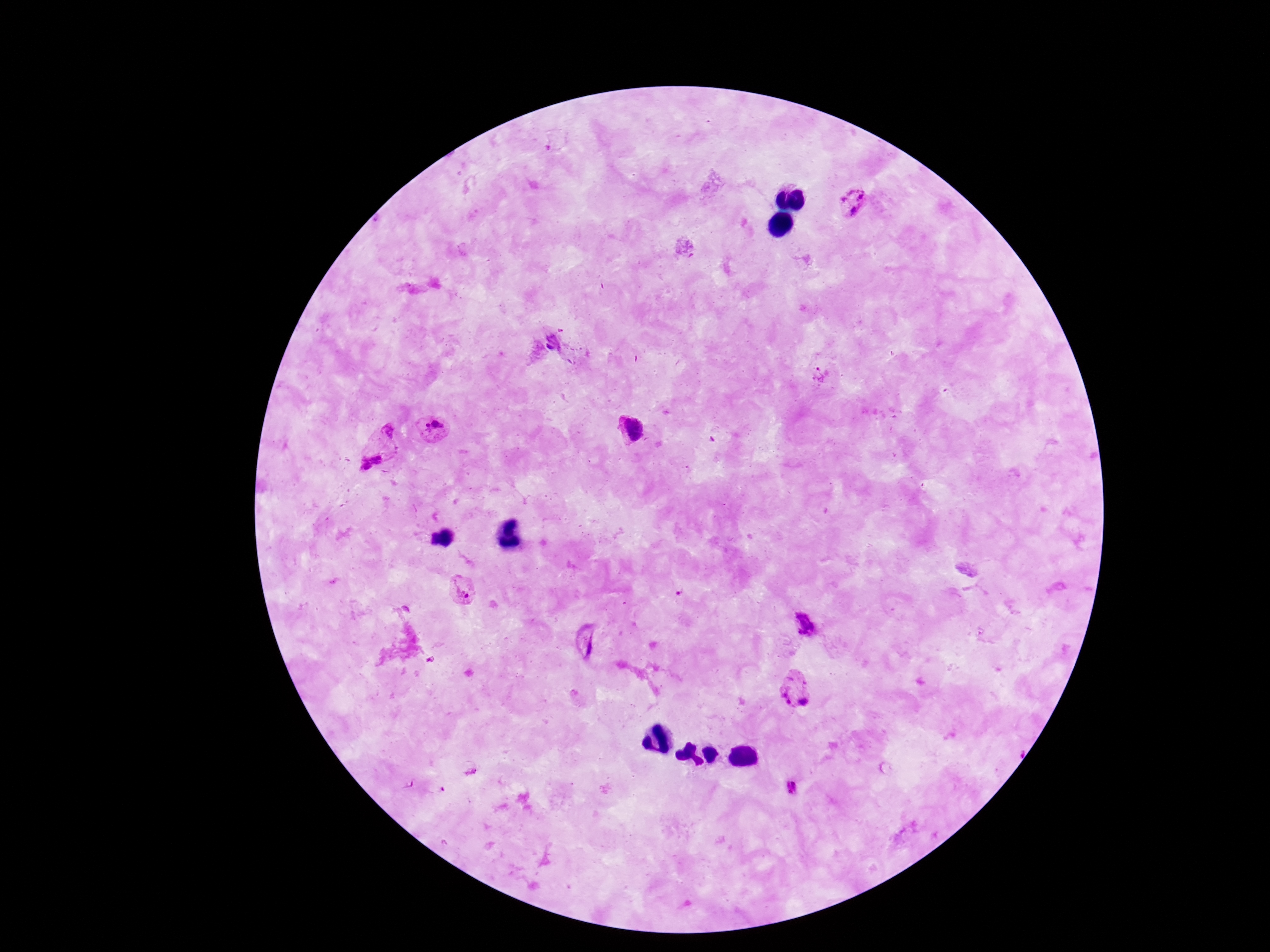
Plasmodium parasite locations = approximate centers as (x, y) in pixels: (851, 203), (821, 376), (435, 429), (629, 429), (377, 446), (463, 592), (804, 624), (588, 642), (795, 689), (470, 769), (792, 789)
magnification = 100x
preparation = thick peripheral-blood smear
capture = smartphone camera through the microscope eyepiece
patient malaria status = infected
stain = Giemsa
field of view = one from this slide
image size = 1270×952 pixels